Give the position of every malaria parasite.
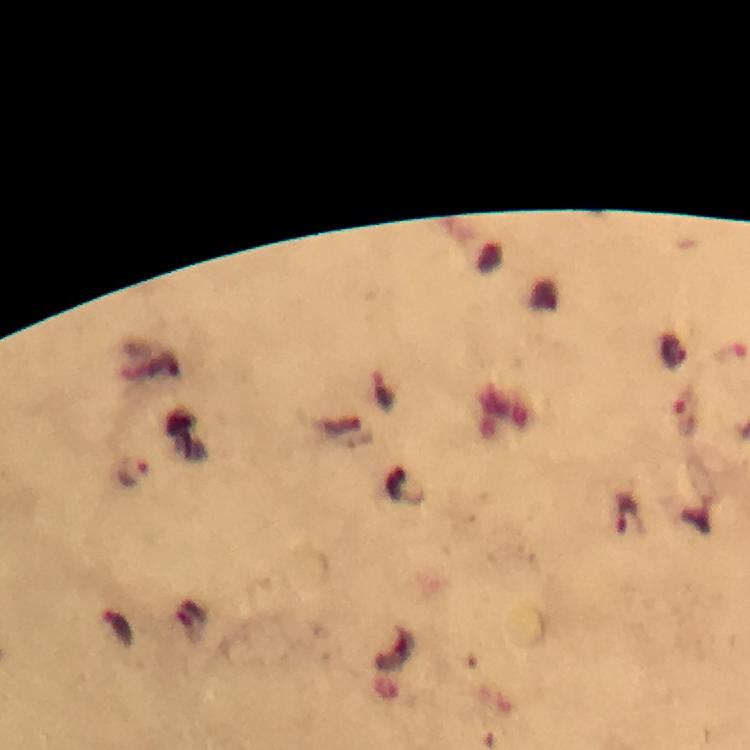
Approximate centers as (x, y) in pixels.
Malaria parasites: (685, 417), (133, 473), (629, 516), (118, 629).

100x magnification. From a diagnostic examination for malaria. Immersion oil applied. Cropped region of a single field of view. Smartphone photograph taken through a microscope. Giemsa stain. Thick blood smear. Image is 750×750 pixels.